Assess this cell for malaria.
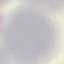
It is uninfected.

Giemsa-stained preparation. Thin blood smear. Automatically extracted cell patch, resized to 64 × 64 pixels. Photographed with a smartphone camera at the microscope eyepiece.